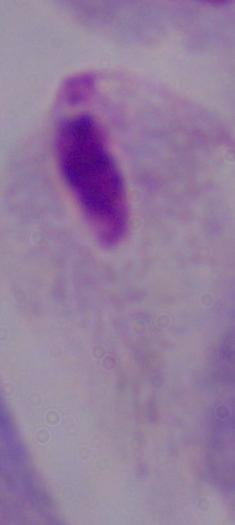
Summary:
  - Modality: photomicrograph
  - Identification: trichomonad
  - Magnification: 1000x